Assess this cell for malaria.
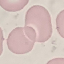
Uninfected.

stain = Giemsa
preparation = thin smear
image type = automatically extracted cell patch, resized to 64 × 64 pixels
capture = smartphone camera at the microscope eyepiece